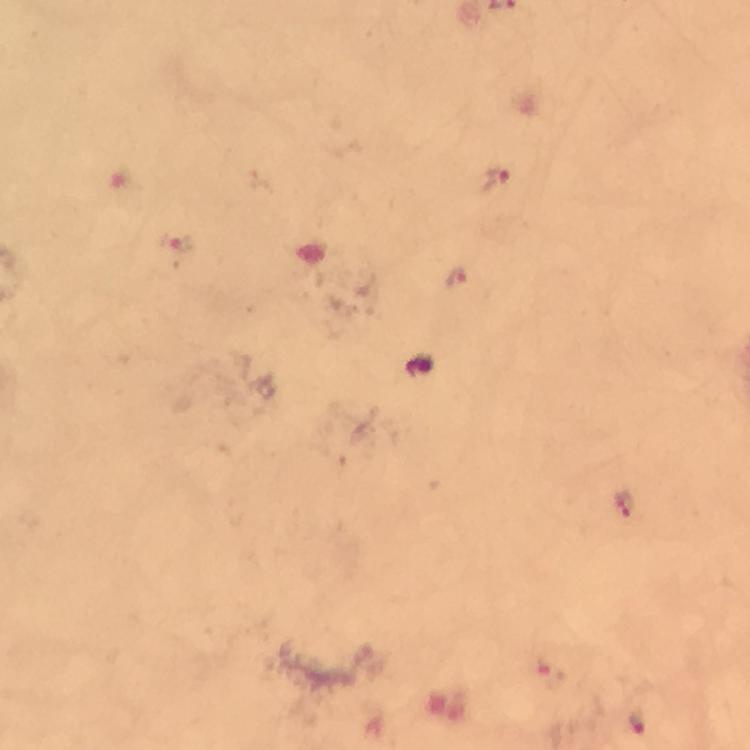
Approximate centers as (x, y) in pixels.
Summary:
  - Malaria parasite locations: (497, 180), (175, 242), (458, 278), (626, 506), (550, 675), (639, 723)
  - Image size: 750×750 pixels
  - Cropped from: a single field of view
  - Magnification: 100x
  - Capture: smartphone photograph through a microscope
  - Context: from a malaria diagnostic workup
  - Preparation: thick blood smear
  - Immersion oil: applied
  - Stain: Giemsa